Report the malaria status of this cell.
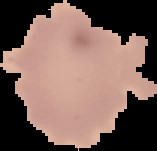

It is uninfected.

Summary:
  - Image type: segmented cell region with the area outside set to black
  - Image size: 157×151 pixels
  - Preparation: thin blood film